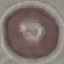

Result: no malaria parasites seen. Acquired by smartphone through the microscope eyepiece. Thin blood film. Giemsa stain. Automatically extracted cell patch, resized to 64 × 64 pixels.